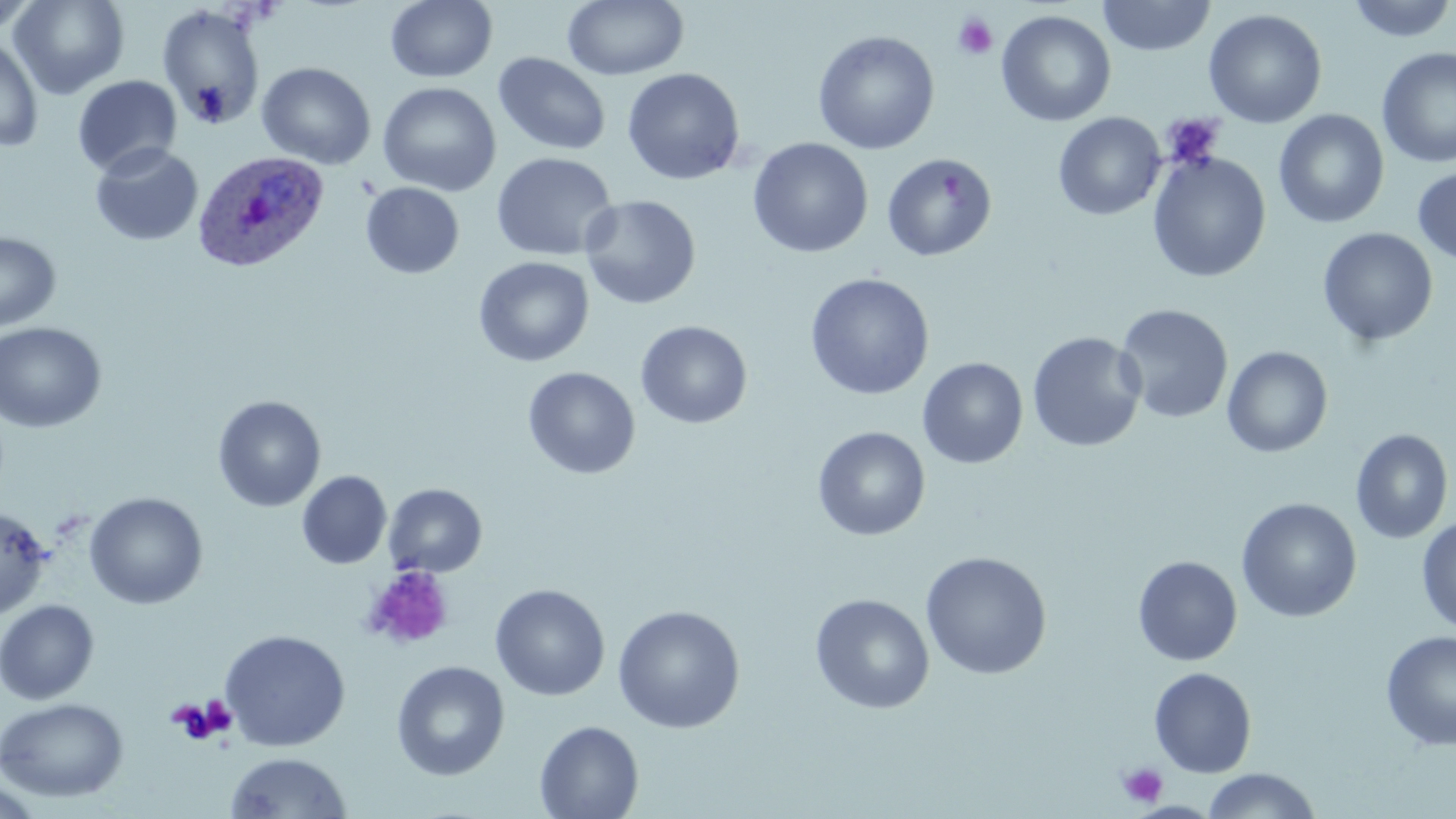

{
  "slide_level_diagnosis": "Plasmodium ovale",
  "stain": "May-Grünwald-Giemsa",
  "platelet_locations": "approximate bounding boxes as (x1, y1, x2, y2) in pixels: (952, 13, 998, 60), (1160, 113, 1225, 171), (364, 565, 454, 651), (169, 698, 233, 744), (1117, 762, 1167, 808)",
  "plasmodium_ovale_infected_red_blood_cell_locations": "approximate bounding boxes as (x1, y1, x2, y2) in pixels: (193, 150, 329, 272)",
  "field_of_view": "single",
  "uninfected_red_blood_cell_locations": "approximate bounding boxes as (x1, y1, x2, y2) in pixels: (0, 0, 40, 35), (9, 0, 129, 99), (562, 0, 690, 81), (1097, 0, 1216, 57), (1345, 0, 1455, 43), (385, 1, 498, 83), (157, 5, 266, 131), (1203, 8, 1328, 129), (996, 9, 1116, 127), (812, 29, 940, 155), (0, 35, 43, 153), (1377, 46, 1456, 168), (493, 52, 612, 156), (257, 62, 376, 169), (622, 67, 745, 185), (72, 75, 182, 177), (378, 82, 501, 196), (1273, 109, 1390, 228), (1052, 112, 1166, 221), (748, 137, 873, 258), (90, 142, 203, 246), (1147, 151, 1272, 283), (491, 152, 617, 262), (881, 152, 998, 262), (1413, 166, 1456, 265), (360, 182, 465, 279), (580, 195, 701, 309), (1318, 227, 1438, 347), (0, 231, 61, 333), (473, 256, 594, 367), (804, 273, 935, 401), (1114, 304, 1234, 424), (636, 320, 752, 429), (0, 321, 107, 433), (1027, 331, 1147, 452), (1222, 346, 1333, 458), (917, 357, 1028, 469), (523, 366, 640, 480), (212, 395, 326, 512), (812, 426, 931, 541), (1350, 428, 1454, 544), (297, 471, 392, 569), (383, 483, 488, 578), (84, 491, 208, 609), (1236, 497, 1362, 623), (0, 505, 52, 620), (1416, 518, 1456, 633), (919, 551, 1053, 680), (1132, 556, 1242, 665), (490, 583, 610, 701), (809, 593, 934, 714), (0, 599, 99, 704), (612, 604, 746, 733), (219, 629, 351, 752), (1381, 630, 1456, 752), (391, 660, 510, 781), (1149, 667, 1257, 778), (1, 697, 128, 802), (534, 720, 644, 819), (225, 752, 352, 818), (1202, 768, 1322, 819), (0, 779, 47, 817)",
  "magnification": "1000x",
  "preparation": "thin blood smear",
  "modality": "optical microscopy",
  "image_size": "1456×819 pixels"
}